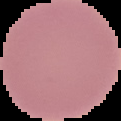 Result: no Plasmodium parasites seen. From a thin blood smear. The area outside the segmented cell region is set to black. Image is 121×121 pixels.